Classify this cell by malaria status.
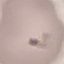
Uninfected.

stain = Giemsa
capture = smartphone through the microscope eyepiece
preparation = thin blood film
image type = cell patch, automatically extracted from a larger field of view and resized to 64 × 64 pixels